Assess this cell for malaria.
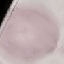
Uninfected.

Thin smear of blood. Acquired by smartphone through the microscope eyepiece. Giemsa-stained preparation. Automatically extracted cell patch, resized to 64 × 64 pixels.